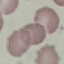
{
  "result": "negative for malaria parasites",
  "image_type": "cell patch, automatically extracted from a larger field of view and resized to 64 × 64 pixels",
  "preparation": "thin blood film",
  "capture": "smartphone through the microscope eyepiece",
  "stain": "Giemsa"
}